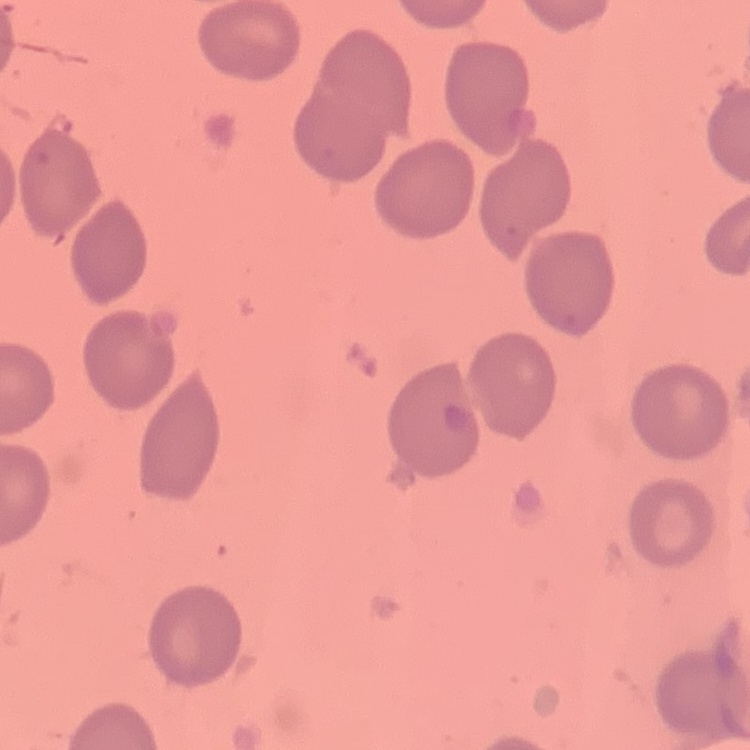

The erythrocytes show no rouleaux formation. One tile cut from a larger photomicrograph. Thin peripheral smear. Field's or Giemsa stain.